Classify this cell by malaria status.
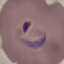
Parasitized.

Summary:
  - Capture: smartphone camera at the microscope eyepiece
  - Stain: Giemsa
  - Image type: automatically extracted cell patch, resized to 64 × 64 pixels
  - Preparation: thin blood film